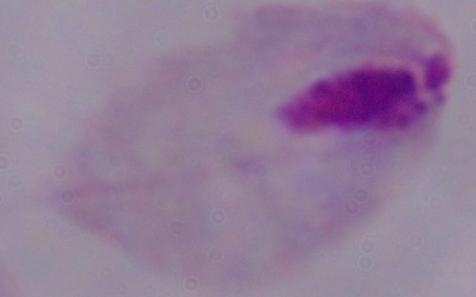 Captured at 1000x magnification. A trichomonad is shown. Photomicrograph.